Give the position of every malaria parasite.
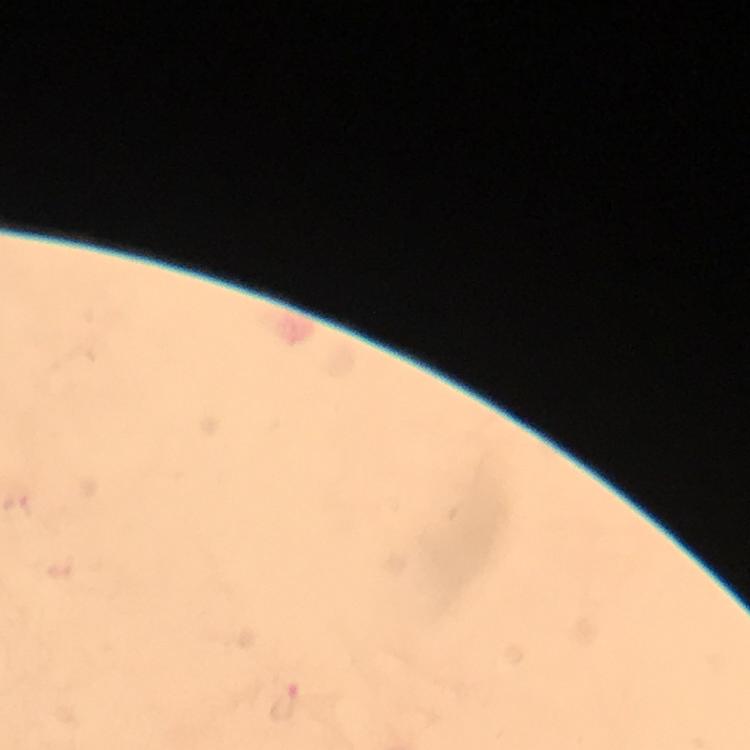
Approximate centers as {x, y} in pixels.
Malaria parasites: {283, 701}.

At 100x magnification. Image is 750×750 pixels. Photographed through the microscope with a smartphone camera. Cropped region of a single field of view. Immersion oil applied. Giemsa stain. From a malaria diagnostic workup. Thick blood smear.